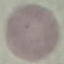
Result: negative for malaria parasites. Thin blood smear. Cell patch, automatically extracted from a larger field of view and resized to 64 × 64 pixels. Acquired by smartphone through the microscope eyepiece. Giemsa-stained preparation.